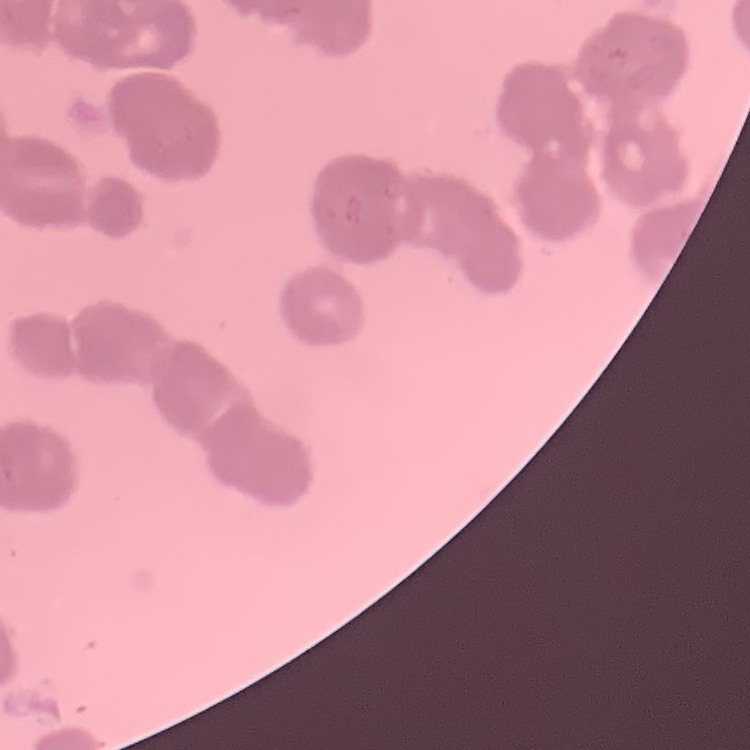

{
  "red_blood_cell_morphology": "rouleaux formation",
  "image_type": "square crop of a larger photomicrograph",
  "stain": "Field's or Giemsa",
  "preparation": "thin blood film"
}